Name the parasite shown.
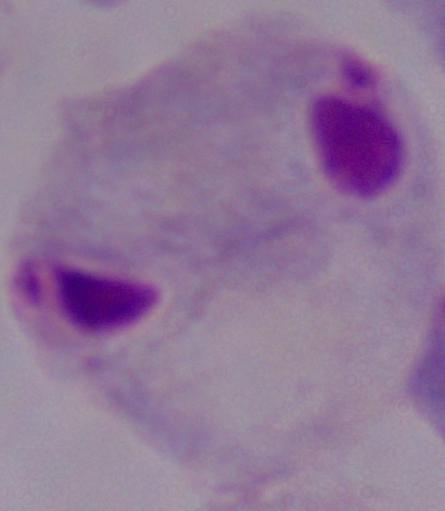
This is a trichomonad.

modality = photomicrograph
magnification = 1000x